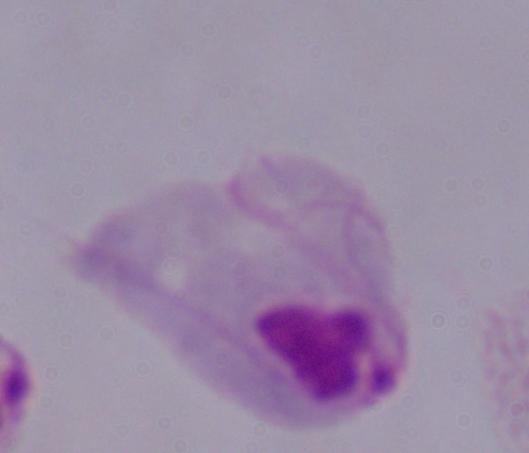
Photomicrograph. A trichomonad is seen. Captured at 1000x magnification.